Describe the morphology of the red blood cells.
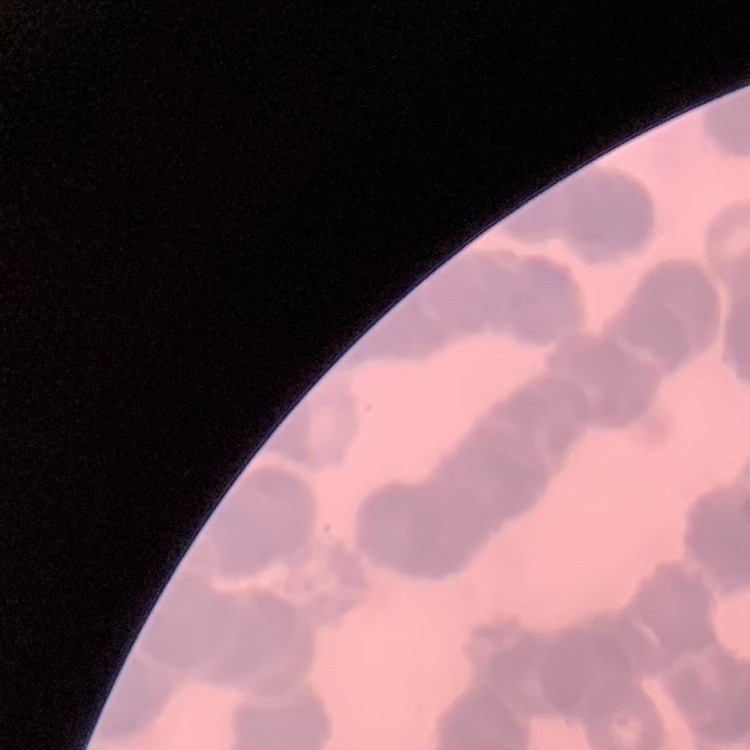

Rouleaux formation.

Summary:
  - Image type: one tile cut from a larger photomicrograph
  - Preparation: thin blood film
  - Stain: Field's or Giemsa